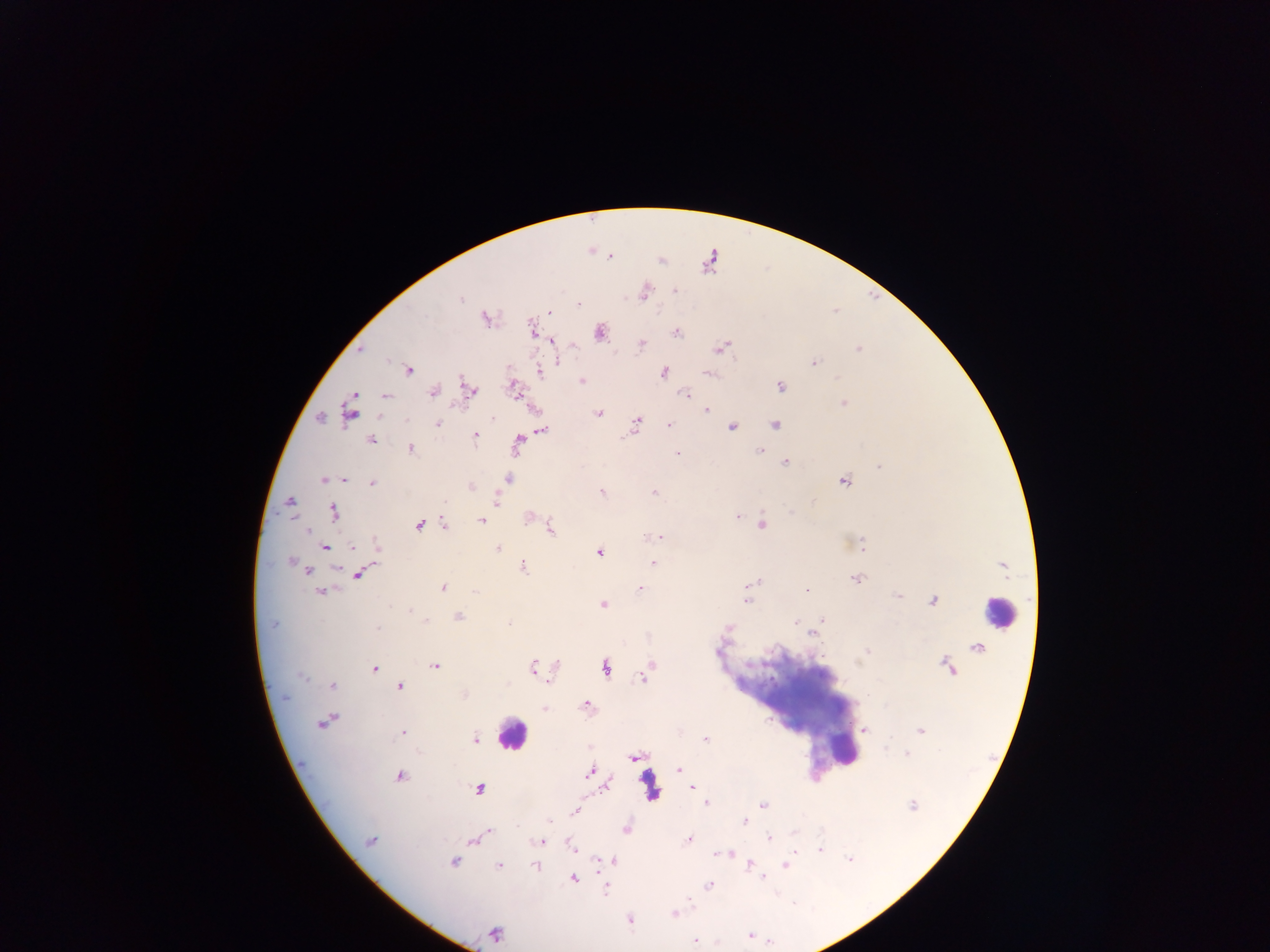 Approximate centers as (x, y) in pixels. Malaria parasite locations: (609, 256), (674, 291), (644, 292), (461, 299), (578, 304), (550, 312), (485, 319), (533, 331), (600, 332), (677, 333), (552, 341), (641, 343), (721, 348), (361, 349), (858, 349), (559, 362), (813, 363), (408, 370), (664, 372), (540, 373), (709, 373), (582, 381), (780, 386), (514, 389), (468, 390), (434, 392), (686, 395), (354, 396), (386, 396), (843, 403), (706, 410), (348, 413), (599, 413), (320, 418), (493, 418), (636, 421), (438, 424), (775, 424), (669, 425), (733, 427), (543, 430), (475, 436), (371, 440), (518, 443), (411, 448), (759, 451), (677, 454), (785, 462), (878, 466), (508, 479), (323, 480), (346, 480), (844, 481), (372, 483), (471, 487), (602, 492), (654, 492), (496, 499), (290, 501), (445, 501), (812, 501), (333, 512), (790, 513), (737, 516), (528, 517), (481, 521), (420, 525), (763, 525), (445, 526), (307, 530), (551, 530), (650, 537), (661, 537), (378, 545), (862, 545), (324, 547), (352, 548), (498, 548), (599, 553), (291, 561), (653, 563), (524, 567), (337, 570), (307, 571), (358, 575), (856, 579), (758, 581), (749, 584), (443, 588), (639, 588), (807, 590), (475, 591), (321, 592), (897, 596), (933, 600), (747, 601), (604, 605), (410, 611), (458, 616), (822, 619), (427, 621), (796, 622), (509, 623), (819, 624), (272, 625), (378, 627), (729, 628), (812, 634), (867, 651), (435, 666), (533, 666), (374, 668), (606, 668), (645, 673), (302, 677), (643, 677), (333, 685), (401, 686), (464, 695), (586, 705), (544, 708), (325, 722), (864, 731), (920, 731), (403, 732), (475, 739), (706, 739), (885, 747), (907, 754), (633, 757), (679, 770), (589, 771), (400, 776), (607, 784), (691, 788), (479, 789), (706, 803), (912, 805), (762, 806), (574, 812), (745, 821), (517, 826), (626, 829), (488, 831), (769, 838), (474, 840), (688, 840), (370, 841), (541, 841), (572, 847), (820, 849), (795, 851), (730, 854), (716, 855), (849, 859), (598, 861), (614, 861), (453, 862), (749, 865), (785, 865), (499, 866), (535, 866), (764, 877), (574, 878), (709, 885), (606, 891), (689, 898), (674, 913), (630, 920), (495, 934), (749, 936), (695, 941). Leukocyte locations: (998, 611), (511, 735), (838, 747). Thick blood film. Mobile-phone photograph taken through the microscope. Image is 1270×952 pixels. One field of view. Sample from Ghana.